Evaluate for malaria.
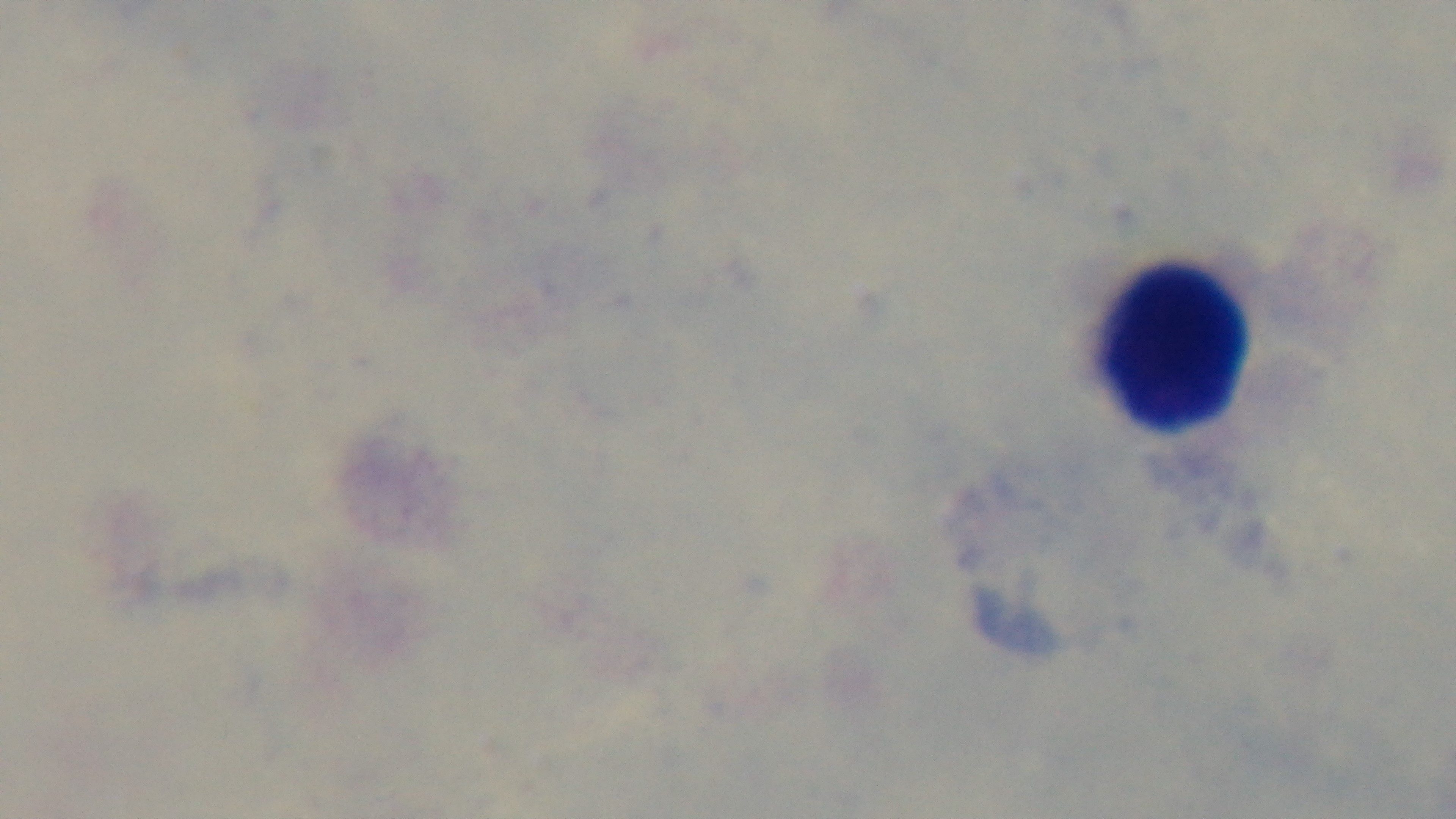
Uninfected.

capture = mounted 4K digital camera
objective = 100x oil immersion
field of view = single
stain = Giemsa
modality = light microscopy
preparation = thick blood film